Look for Plasmodium parasites.
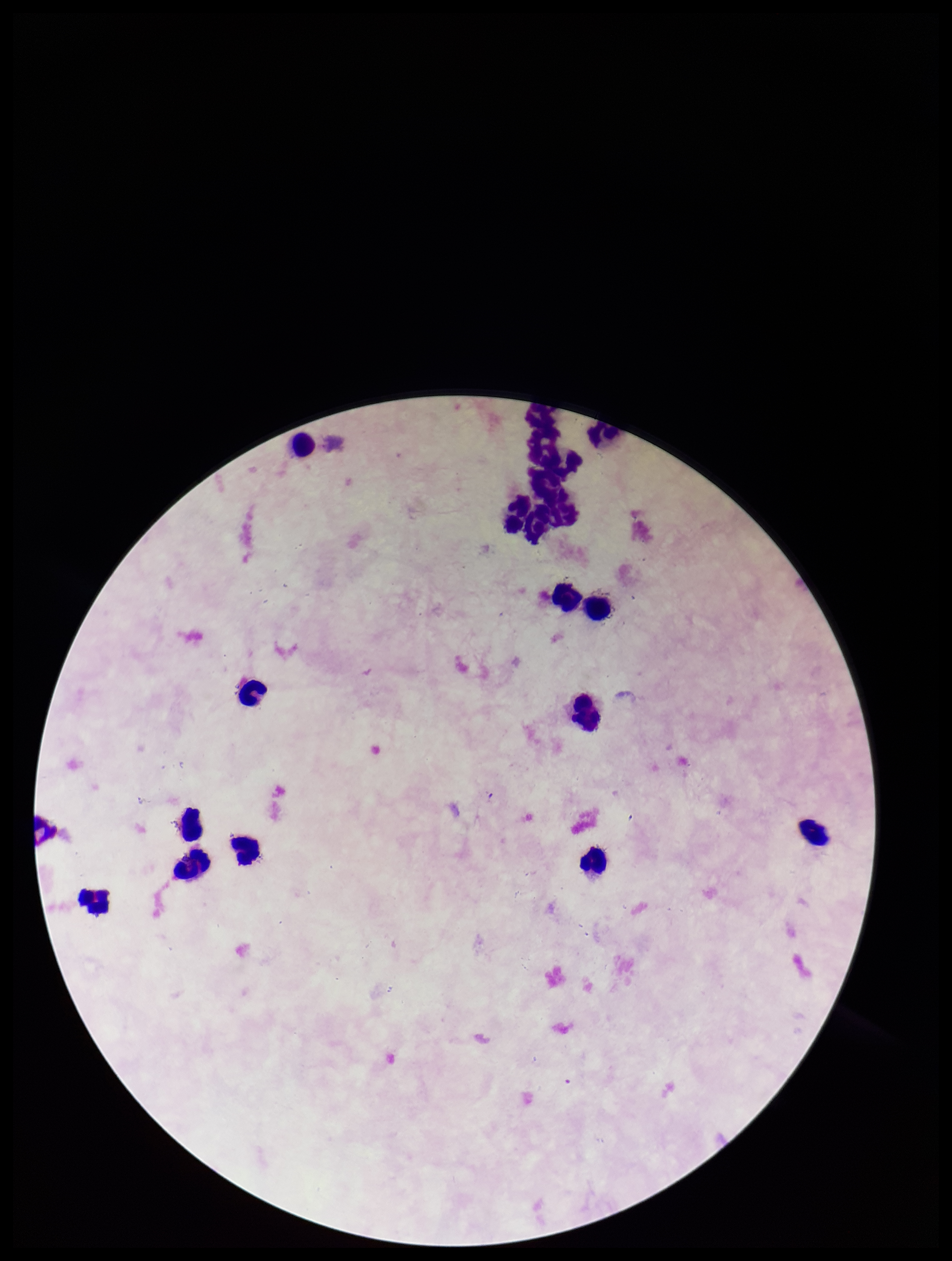

None seen.

Summary:
  - Stain: Giemsa
  - Image size: 952×1261 pixels
  - Leukocyte count: 17
  - Field of view: single
  - Parasite count: 0
  - Capture: smartphone photograph through the microscope eyepiece
  - Patient malaria status: negative
  - Preparation: thick smear